Name the blood parasite species.
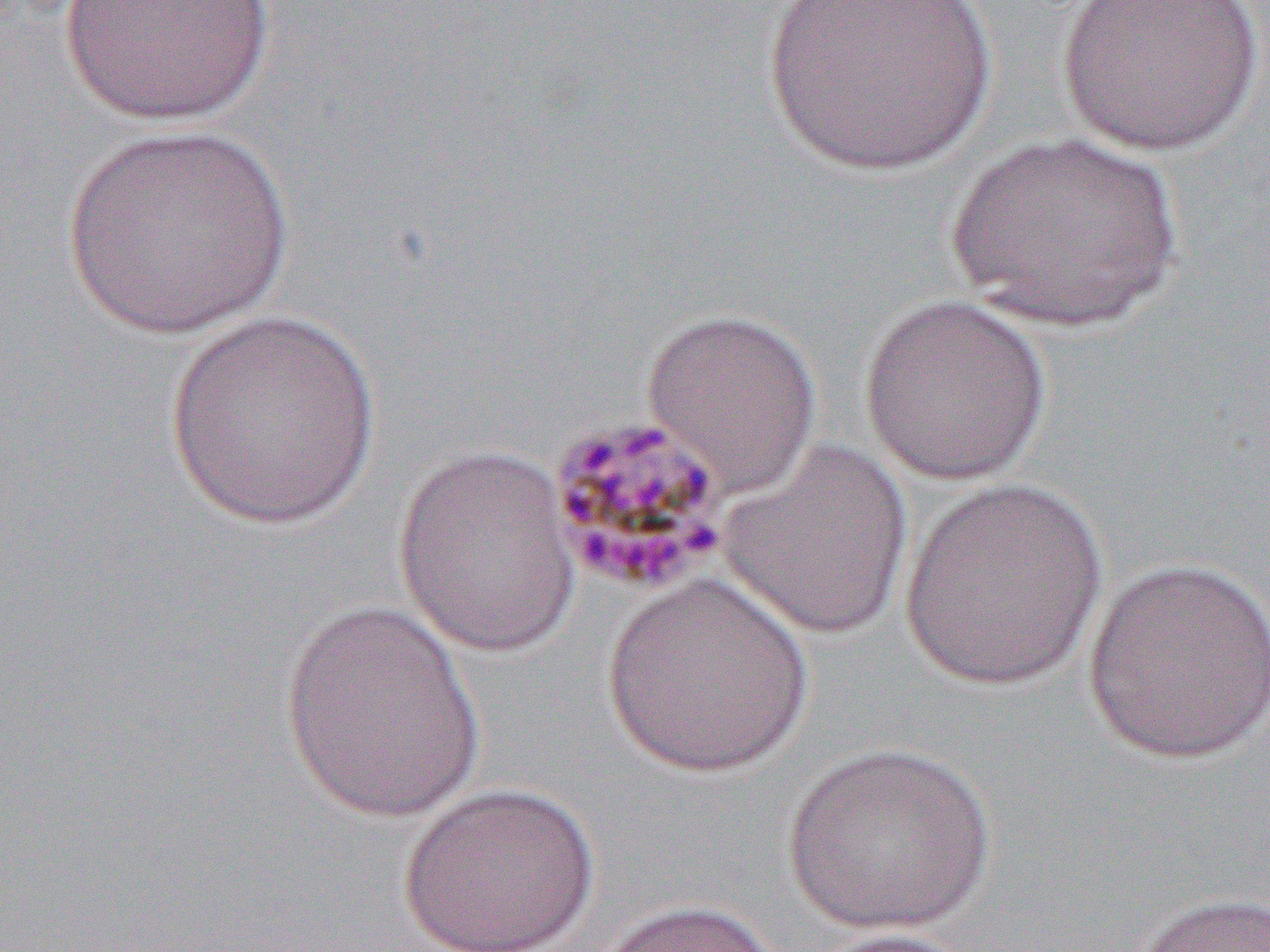
Plasmodium malariae.

preparation = thin blood film
uninfected red blood cell locations = approximate bounding boxes as named x1/y1/x2/y2 corners in pixels: (x1=56, y1=0, x2=279, y2=126), (x1=1055, y1=0, x2=1264, y2=156), (x1=756, y1=1, x2=1001, y2=179), (x1=61, y1=124, x2=294, y2=340), (x1=940, y1=129, x2=1190, y2=334), (x1=857, y1=293, x2=1054, y2=485), (x1=640, y1=305, x2=823, y2=496), (x1=161, y1=310, x2=384, y2=533), (x1=715, y1=437, x2=915, y2=641), (x1=391, y1=446, x2=583, y2=658), (x1=898, y1=476, x2=1108, y2=691), (x1=1081, y1=555, x2=1270, y2=766), (x1=599, y1=573, x2=816, y2=778), (x1=277, y1=600, x2=492, y2=824), (x1=780, y1=740, x2=996, y2=935), (x1=397, y1=781, x2=600, y2=952), (x1=1124, y1=889, x2=1270, y2=952), (x1=588, y1=897, x2=791, y2=952), (x1=804, y1=926, x2=987, y2=951)
Plasmodium malariae-infected red blood cell locations = approximate bounding boxes as named x1/y1/x2/y2 corners in pixels: (x1=543, y1=412, x2=734, y2=597)
magnification = 1000x
image size = 1270×952 pixels
modality = optical microscopy
field of view = single